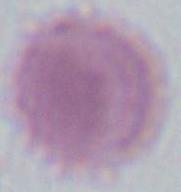

Summary:
  - Modality: photomicrograph
  - Identification: red blood cell
  - Magnification: 1000x